Report the malaria status of this cell.
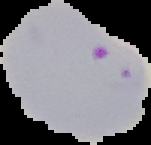

Parasitized.

Summary:
  - Preparation: thin blood film
  - Image size: 151×145 pixels
  - Image type: segmented cell region on a black background